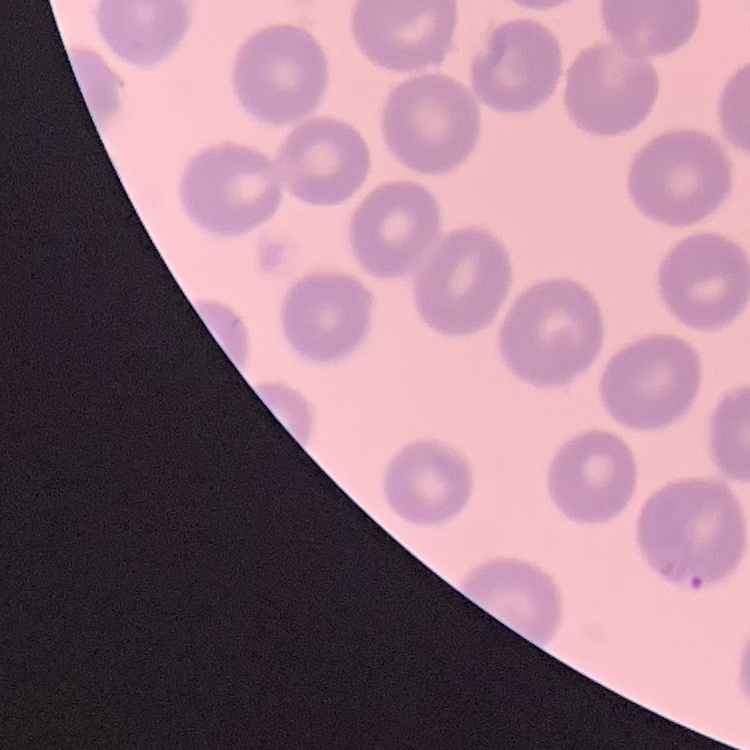 The red blood cells exhibit no rouleaux formation. Field's or Giemsa stain. Thin blood smear. One tile cut from a larger photomicrograph.